Give the extent of all white blood cells.
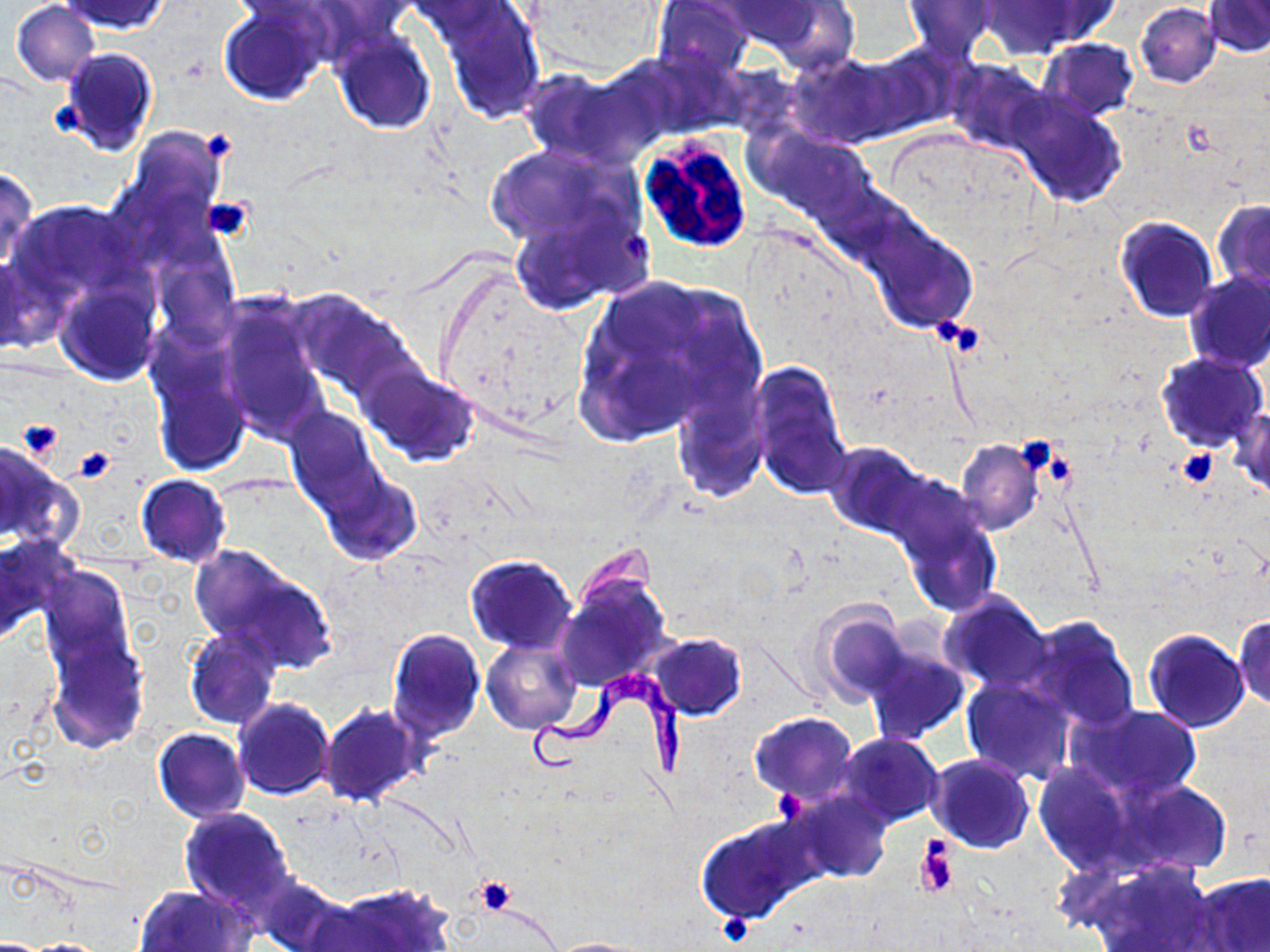

Approximate bounding boxes as [x1, y1, x2, y2] in pixels.
White blood cells: [638, 134, 751, 255].

slide-level diagnosis = Trypanosoma brucei
modality = optical microscopy
Trypanosoma brucei locations = approximate bounding boxes as [x1, y1, x2, y2] in pixels: [524, 672, 689, 780]
stain = May-Grünwald-Giemsa
platelet locations = approximate bounding boxes as [x1, y1, x2, y2] in pixels: [53, 105, 83, 134], [198, 130, 237, 164], [203, 195, 253, 242], [623, 235, 652, 265], [933, 316, 958, 345], [958, 324, 982, 356], [18, 419, 66, 462], [1013, 437, 1060, 478], [73, 445, 116, 482], [1039, 447, 1077, 491], [1176, 449, 1219, 488], [772, 789, 806, 820], [917, 842, 957, 897], [475, 877, 517, 916], [718, 912, 756, 946]
preparation = thin blood smear
uninfected red blood cell locations = approximate bounding boxes as [x1, y1, x2, y2] in pixels: [59, 0, 170, 35], [652, 0, 754, 79], [718, 1, 826, 52], [756, 1, 862, 72], [902, 1, 996, 59], [979, 1, 1102, 55], [1203, 1, 1270, 58], [10, 2, 100, 86], [1135, 3, 1221, 88], [219, 4, 330, 105], [436, 5, 545, 124], [331, 30, 437, 135], [1039, 38, 1138, 121], [58, 47, 159, 155], [790, 54, 901, 148], [947, 59, 1050, 155], [521, 69, 651, 166], [1008, 91, 1126, 208], [124, 126, 228, 226], [751, 126, 877, 225], [482, 143, 635, 250], [0, 164, 39, 274], [1213, 200, 1270, 293], [9, 201, 138, 301], [509, 208, 640, 314], [1116, 216, 1217, 322], [863, 218, 979, 333], [1, 252, 39, 358], [154, 255, 239, 347], [1183, 270, 1270, 372], [574, 275, 765, 442], [56, 283, 161, 385], [292, 292, 415, 397], [218, 303, 329, 444], [146, 346, 251, 478], [1156, 352, 1269, 451], [749, 361, 851, 499], [357, 364, 483, 469], [670, 382, 770, 505], [285, 408, 386, 515], [1230, 408, 1270, 502], [1010, 438, 1062, 476], [955, 439, 1043, 535], [826, 441, 927, 538], [0, 446, 76, 552], [135, 474, 231, 568], [321, 474, 421, 566], [890, 493, 1002, 618], [0, 535, 77, 645], [188, 546, 326, 664], [465, 554, 578, 653], [38, 566, 134, 674], [555, 574, 672, 693], [937, 591, 1051, 694], [808, 598, 909, 706], [1233, 614, 1270, 711], [1019, 615, 1140, 733], [44, 627, 150, 754], [183, 627, 280, 730], [386, 628, 487, 742], [1143, 629, 1249, 732], [647, 633, 747, 720], [483, 639, 583, 735], [860, 642, 972, 746], [961, 674, 1077, 785], [233, 697, 334, 800], [319, 703, 427, 807], [1074, 703, 1203, 801], [749, 711, 860, 803], [153, 727, 249, 822], [837, 733, 943, 828], [926, 756, 1035, 854], [1032, 762, 1137, 873], [1111, 778, 1230, 877], [785, 788, 894, 884], [179, 807, 295, 913], [694, 814, 820, 923], [1089, 861, 1225, 952], [1192, 872, 1270, 951], [254, 875, 348, 952], [326, 883, 455, 952], [134, 886, 254, 952], [546, 937, 651, 952]
field of view = one of a larger specimen
magnification = 1000x
image size = 1270×952 pixels